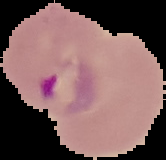
preparation: thin blood smear
image_size: 166×160 pixels
malaria_status: parasitized
image_type: segmented cell region with the area outside set to black